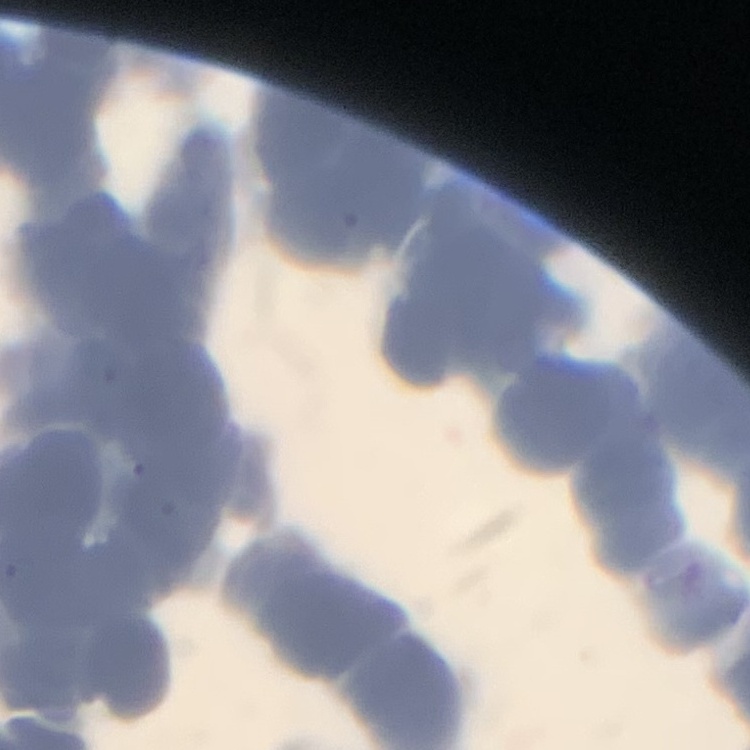
Summary:
  - Red blood cell morphology: rouleaux formation
  - Stain: Field's or Giemsa
  - Image type: one tile cut from a larger photomicrograph
  - Preparation: thin blood film